Report the malaria status of this cell.
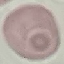

Uninfected.

{
  "stain": "Giemsa",
  "preparation": "thin blood film",
  "capture": "smartphone camera at the microscope eyepiece",
  "image_type": "cell patch, automatically extracted from a larger field of view and resized to 64 × 64 pixels"
}